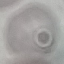
Summary:
  - Malaria status: uninfected
  - Image type: cell patch, automatically extracted from a larger field of view and resized to 64 × 64 pixels
  - Stain: Giemsa
  - Preparation: thin blood smear
  - Capture: smartphone camera at the microscope eyepiece